Assess for Plasmodium parasites.
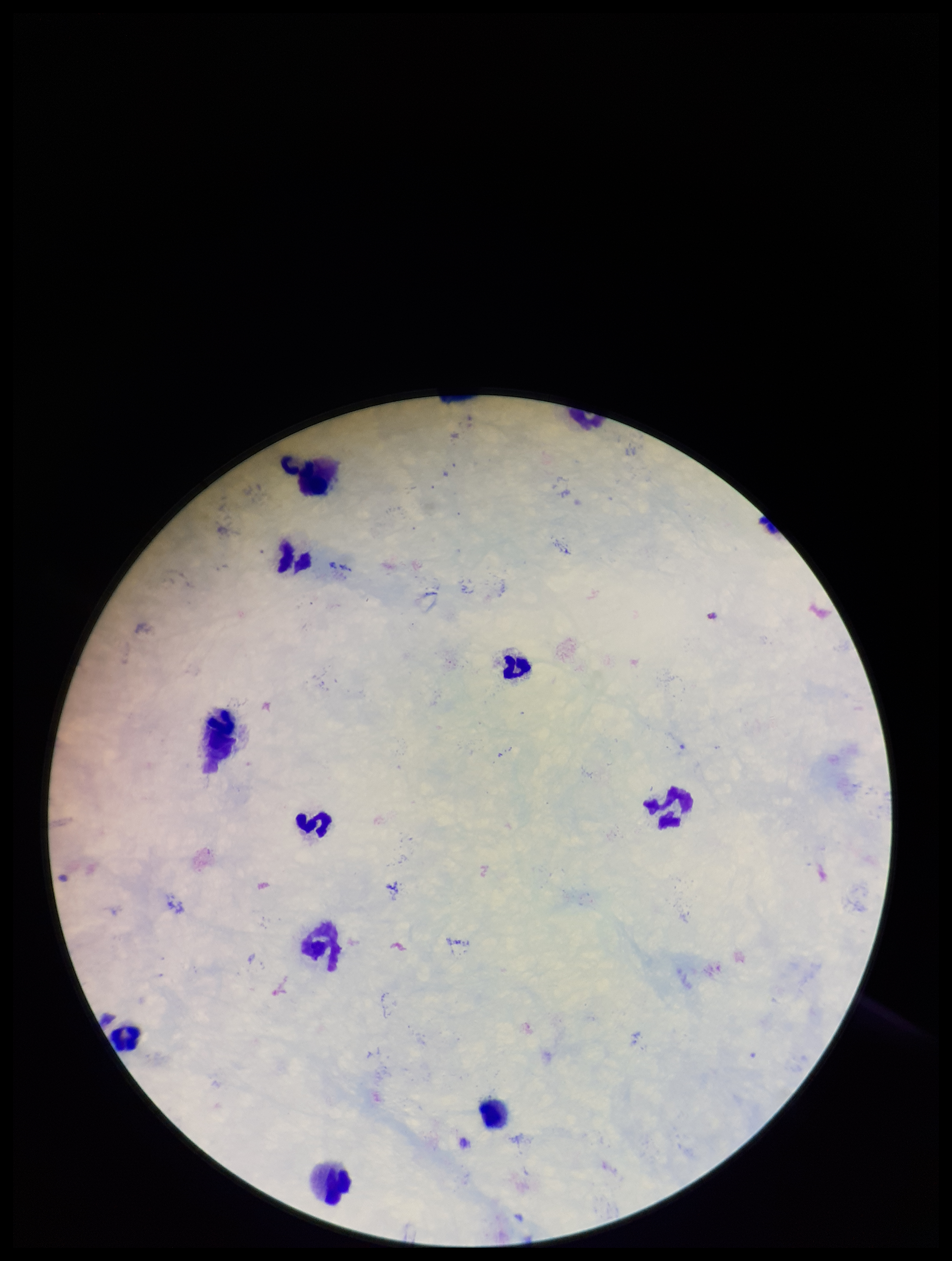

None detected.

Leukocyte count: 9. One field from this slide. Preparation: thick. Stained with Giemsa. Parasite count: 0. Photographed through the microscope eyepiece with a smartphone camera. Image is 952×1261 pixels. Patient malaria status: negative.